Name the parasite shown.
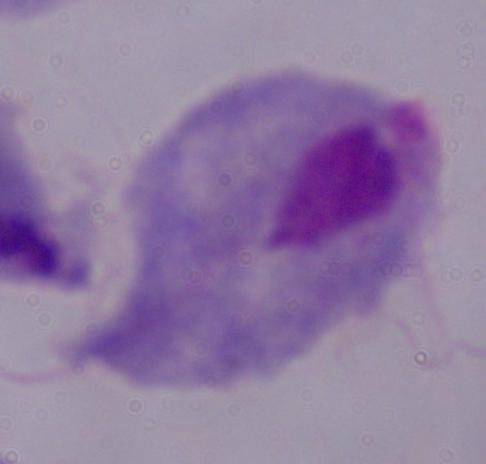

A trichomonad.

{
  "magnification": "1000x",
  "modality": "photomicrograph"
}